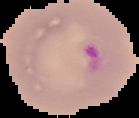
Summary:
  - Image size: 139×118 pixels
  - Preparation: thin blood film
  - Result: malaria parasites identified
  - Image type: cell region segmented out of the field of view; surrounding area masked to black